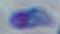

Summary:
  - Modality: micrograph
  - Identification: Toxoplasma gondii
  - Magnification: 1000x